Give the position of every Plasmodium parasite.
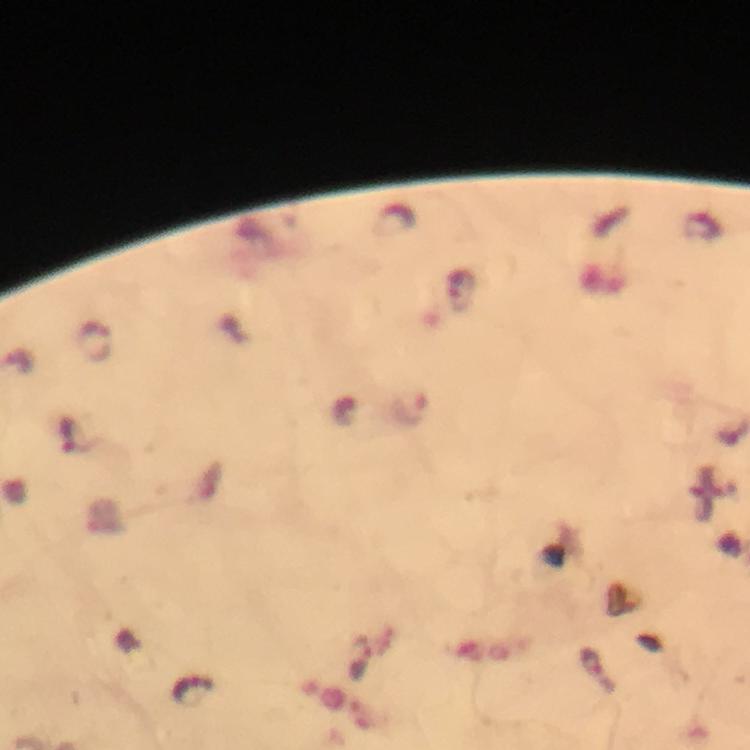

Approximate object centers, in pixels from the top-left corner.
Plasmodium parasites: (x=460, y=292), (x=95, y=343), (x=410, y=409), (x=71, y=436), (x=361, y=660), (x=595, y=669), (x=191, y=691).

Summary:
  - Stain: Giemsa
  - Cropped from: one field of view
  - Image size: 750×750 pixels
  - Context: from a diagnostic examination for malaria
  - Immersion oil: used
  - Preparation: thick smear
  - Magnification: 100x
  - Capture: smartphone camera through the microscope